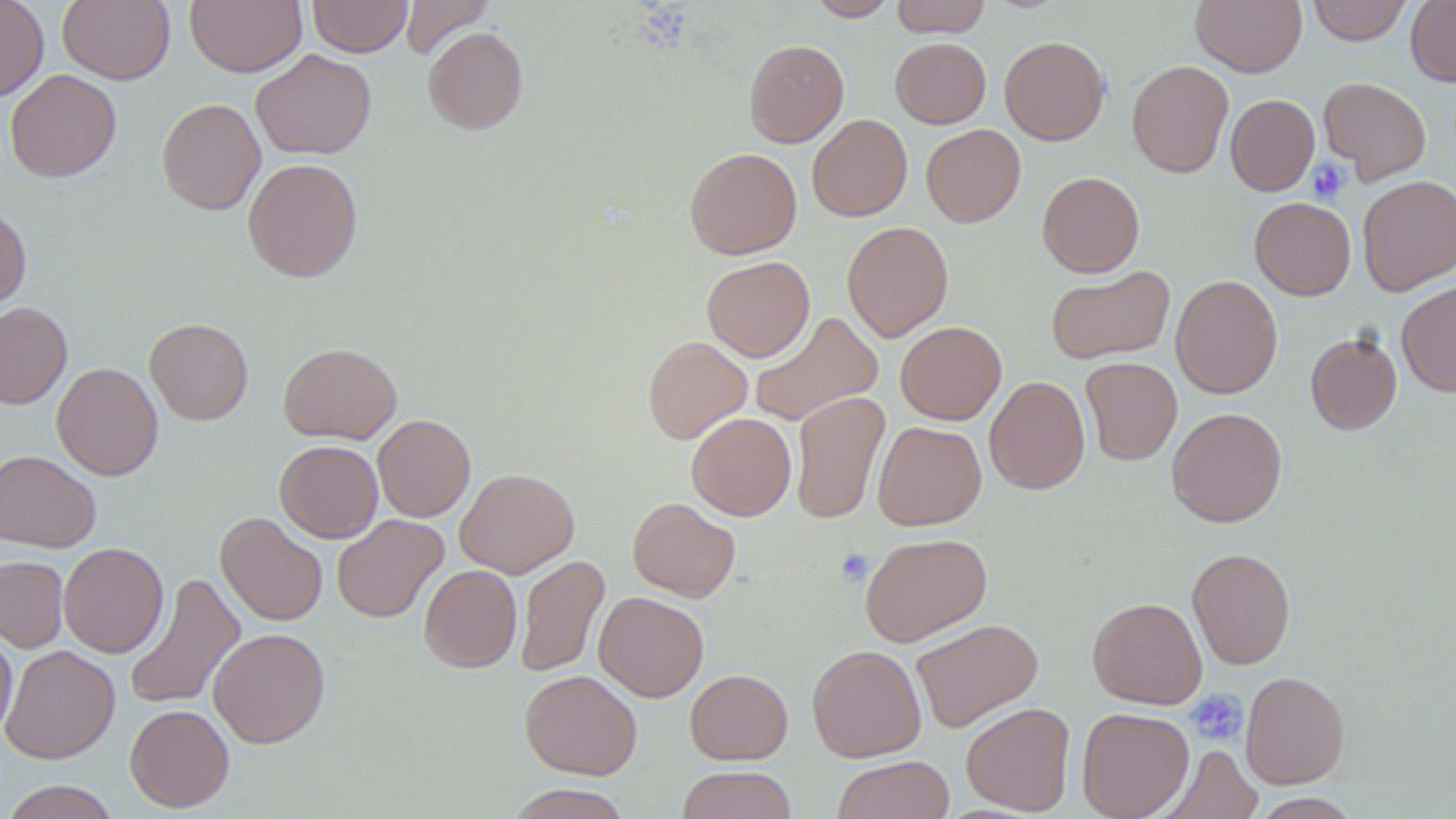

Summary:
  - Coordinate format: approximate bounding boxes as (x1, y1, x2, y2) in pixels
  - Uninfected red blood cell locations: (0, 0, 49, 102), (58, 0, 175, 85), (185, 0, 306, 77), (308, 0, 412, 57), (401, 0, 492, 59), (808, 0, 897, 21), (891, 0, 991, 37), (1191, 0, 1306, 76), (1307, 0, 1412, 45), (1406, 0, 1456, 86), (422, 26, 529, 134), (999, 35, 1110, 145), (890, 37, 991, 128), (744, 39, 848, 147), (251, 49, 376, 160), (1127, 60, 1233, 178), (5, 69, 121, 183), (1318, 77, 1432, 183), (1225, 94, 1320, 196), (156, 97, 266, 215), (807, 114, 912, 221), (921, 124, 1025, 227), (684, 148, 802, 259), (242, 158, 363, 282), (1037, 171, 1145, 277), (1357, 174, 1456, 296), (1249, 197, 1356, 300), (0, 205, 32, 312), (842, 221, 954, 341), (702, 256, 815, 362), (1046, 266, 1175, 365), (1170, 275, 1283, 399), (1396, 280, 1456, 397), (0, 302, 72, 408), (749, 311, 884, 426), (144, 318, 254, 424), (895, 321, 1007, 425), (1305, 332, 1402, 435), (643, 335, 752, 444), (278, 342, 402, 444), (1080, 357, 1182, 465), (52, 362, 164, 480), (984, 375, 1090, 495), (790, 391, 890, 525), (1166, 406, 1287, 527), (686, 413, 796, 521), (372, 414, 475, 522), (872, 421, 986, 530), (274, 440, 383, 542), (0, 449, 101, 552), (454, 467, 580, 578), (628, 497, 740, 602), (215, 512, 328, 626), (332, 514, 449, 623), (859, 532, 992, 647), (59, 542, 169, 658), (1187, 547, 1296, 670), (515, 554, 609, 679), (0, 555, 69, 653), (419, 564, 522, 673), (123, 572, 245, 712), (594, 592, 709, 701), (1087, 596, 1207, 709), (911, 618, 1044, 733), (0, 627, 17, 741), (208, 627, 329, 748), (807, 644, 926, 762), (1, 645, 120, 764), (685, 669, 793, 764), (520, 670, 642, 779), (1240, 670, 1350, 788), (961, 702, 1076, 815), (125, 704, 234, 812), (1076, 707, 1194, 819), (1160, 744, 1263, 819), (832, 755, 955, 819), (676, 766, 797, 819), (1, 780, 121, 818), (506, 783, 631, 819), (1250, 792, 1363, 818)
  - Platelet locations: (1307, 158, 1350, 204), (834, 549, 874, 586), (1186, 690, 1247, 746)
  - Slide-level diagnosis: no evidence of blood parasites
  - Magnification: 1000x
  - Field of view: one of a larger specimen
  - Preparation: thin blood film
  - Image size: 1456×819 pixels
  - Modality: light microscopy
  - Stain: May-Grünwald-Giemsa